Comment on the morphology of the erythrocytes.
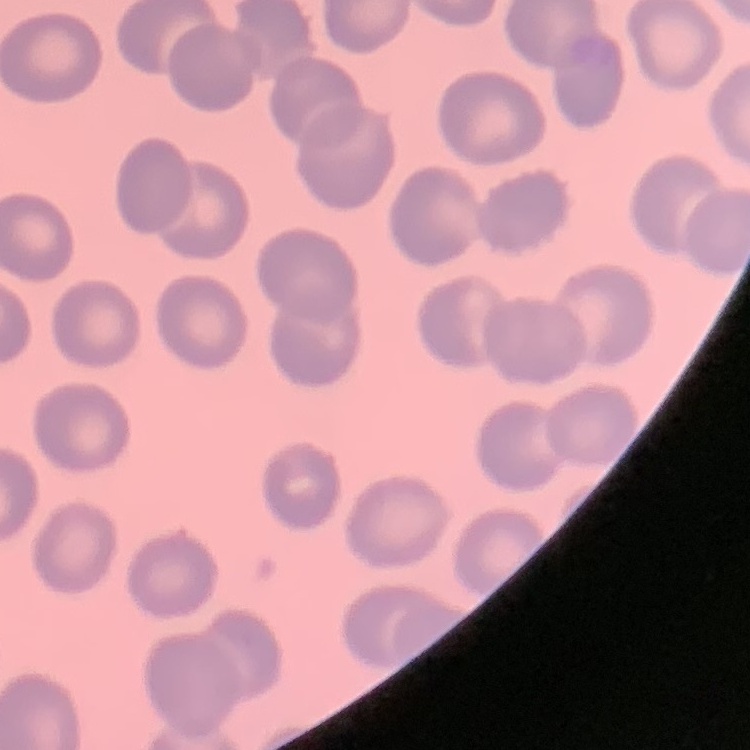

No rouleaux formation.

stain = Field's or Giemsa
image type = one tile cut from a larger photomicrograph
preparation = thin blood film